Assess this cell for malaria.
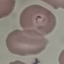

Parasitized.

Thin blood film. Giemsa-stained preparation. Cell patch, automatically extracted from a larger field of view and resized to 64 × 64 pixels. Photographed with a smartphone camera at the microscope eyepiece.